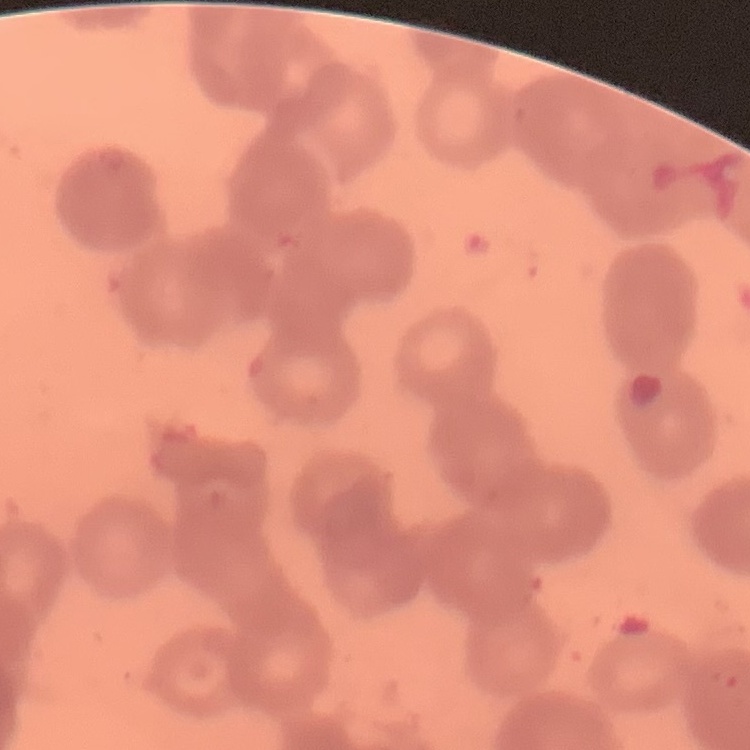
The erythrocytes exhibit rouleaux formation. One tile cut from a larger photomicrograph. Thin blood film. Field's or Giemsa stain.